Describe the morphology of the erythrocytes.
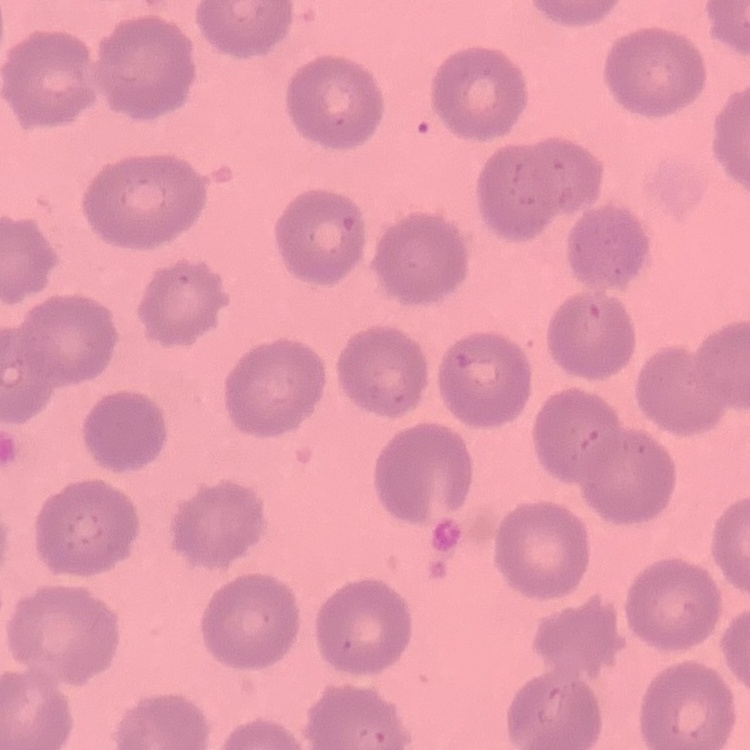
They show no rouleaux formation.

stain = Field's or Giemsa
image type = one tile cut from a larger photomicrograph
preparation = thin blood film